Find each parasitized RBC.
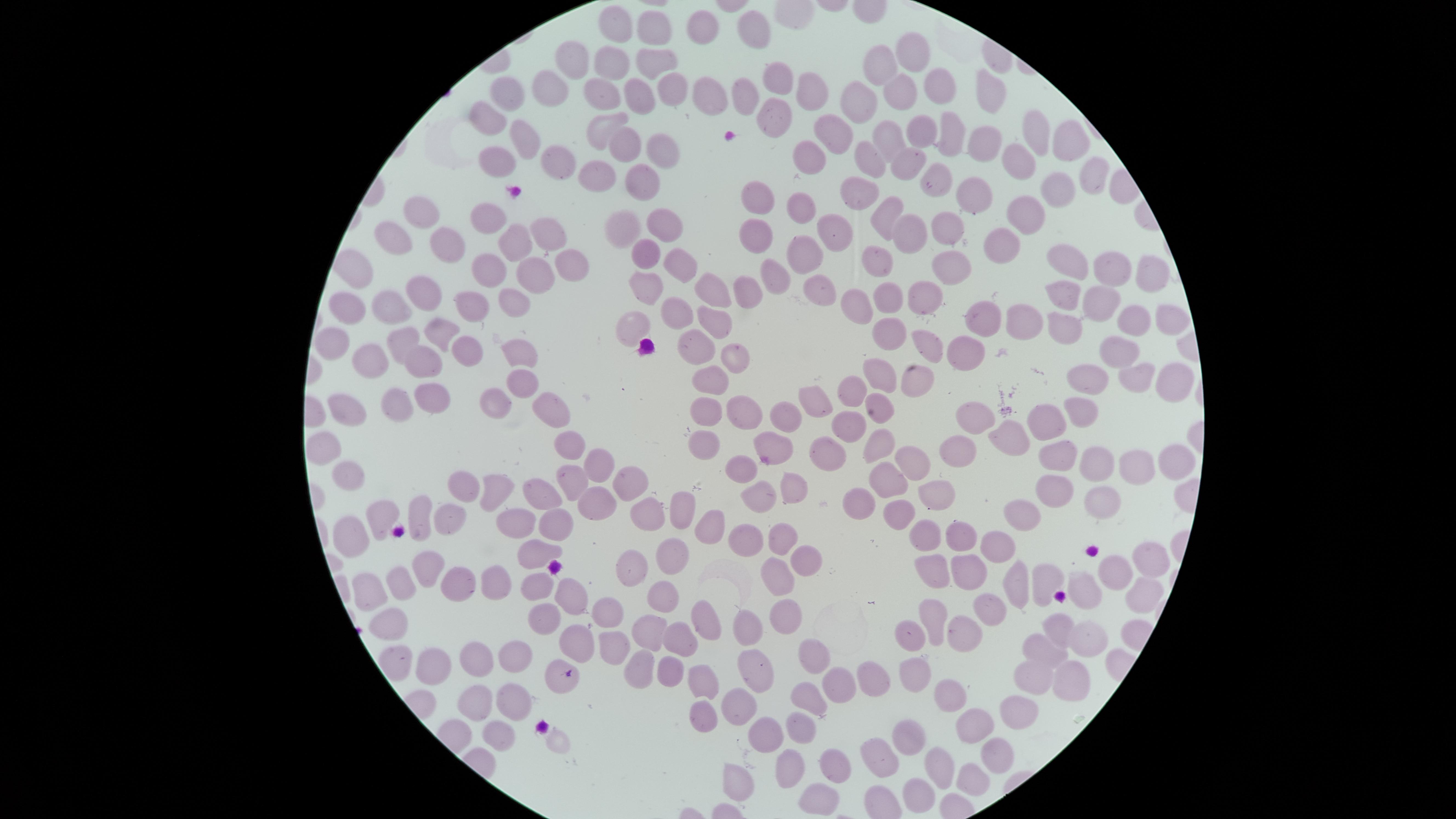

No parasitized RBCs identified.

Approximate marker points as (x, y) in pixels.
Summary:
  - Uninfected RBCs: (620, 23), (702, 24), (754, 25), (659, 29), (917, 51), (655, 54), (573, 57), (614, 68), (881, 68), (777, 80), (936, 80), (675, 84), (550, 86), (811, 87), (995, 88), (606, 93), (508, 94), (636, 94), (710, 94), (900, 95), (745, 96), (859, 105), (771, 113), (487, 114), (831, 126), (603, 128), (524, 129), (1036, 129), (921, 131), (882, 134), (951, 136), (978, 138), (1066, 141), (627, 146), (662, 148), (811, 155), (551, 156), (871, 159), (492, 162), (907, 165), (1021, 167), (601, 174), (1090, 176), (934, 179), (648, 180), (864, 190), (1047, 195), (761, 198), (971, 199), (806, 206), (421, 210), (885, 211), (1023, 212), (953, 218), (488, 219), (665, 223), (625, 226), (831, 229), (905, 230), (543, 232), (757, 235), (1007, 239), (398, 242), (509, 242), (453, 248), (804, 254), (872, 259), (1077, 260), (649, 262), (951, 263), (571, 265), (678, 265), (1116, 268), (358, 270), (487, 271), (537, 271), (1145, 273), (770, 274), (421, 287), (820, 288), (753, 290), (650, 291), (719, 291), (1061, 292), (932, 294), (886, 296), (352, 301), (384, 302), (470, 303), (513, 303), (1094, 305), (856, 309), (718, 316), (678, 317), (984, 318), (1133, 318), (1165, 319), (1021, 320), (1061, 328), (637, 329), (439, 331), (885, 332), (333, 337), (700, 340), (400, 341), (935, 343), (1119, 345), (469, 348), (521, 349), (962, 352), (728, 358), (371, 359), (419, 360), (886, 373), (1082, 373), (715, 378), (1132, 379), (1171, 381), (917, 383), (524, 384), (856, 391), (441, 396), (494, 399), (882, 399), (401, 401), (821, 402), (1074, 404), (710, 407), (738, 407), (342, 408), (786, 410), (980, 411), (553, 415), (1044, 422), (857, 423), (1004, 432), (709, 438), (773, 441), (879, 442), (324, 443), (574, 443), (952, 447), (830, 448), (1068, 450), (913, 456), (1101, 459), (595, 465), (1171, 465), (741, 468), (1138, 468), (351, 473), (896, 474), (1050, 481), (627, 482), (465, 484), (567, 485), (796, 487), (489, 488), (933, 492), (538, 494), (759, 494), (858, 500), (1095, 504), (591, 505), (684, 509), (419, 510), (1034, 512), (447, 513), (640, 513), (897, 514), (513, 520), (713, 520), (552, 524), (387, 525), (746, 533), (351, 534), (958, 534), (780, 535), (925, 537), (1000, 539), (537, 551), (670, 556), (1143, 561), (803, 563), (422, 564), (628, 568), (964, 574), (1109, 574), (399, 577), (1048, 577), (930, 578), (487, 579), (781, 580), (1014, 581), (452, 582), (369, 587), (532, 587), (1092, 593), (666, 595), (569, 596), (1143, 596), (990, 604), (611, 610), (786, 610), (940, 612), (702, 620), (543, 623), (392, 626), (1058, 626), (961, 627), (754, 628), (648, 629), (910, 635), (681, 636), (1085, 638), (580, 642), (613, 643), (1043, 650), (514, 656), (475, 657), (817, 657), (759, 661), (432, 664), (639, 667), (921, 668), (665, 669), (1036, 674), (557, 677), (867, 678), (700, 683), (1066, 685), (833, 686), (956, 690), (811, 698), (478, 701), (511, 705), (739, 708), (700, 711), (1015, 715), (972, 723), (799, 724), (497, 727), (766, 733), (902, 736), (995, 752), (882, 755), (785, 760), (829, 762), (938, 765), (969, 775), (741, 781), (917, 789), (812, 803)
  - Image size: 1456×819 pixels
  - Stain: Giemsa
  - Visible region: circular
  - Capture: smartphone photograph through the microscope eyepiece
  - Field of view: single
  - Preparation: thin blood film